Locate every Plasmodium parasite and every leukocyte.
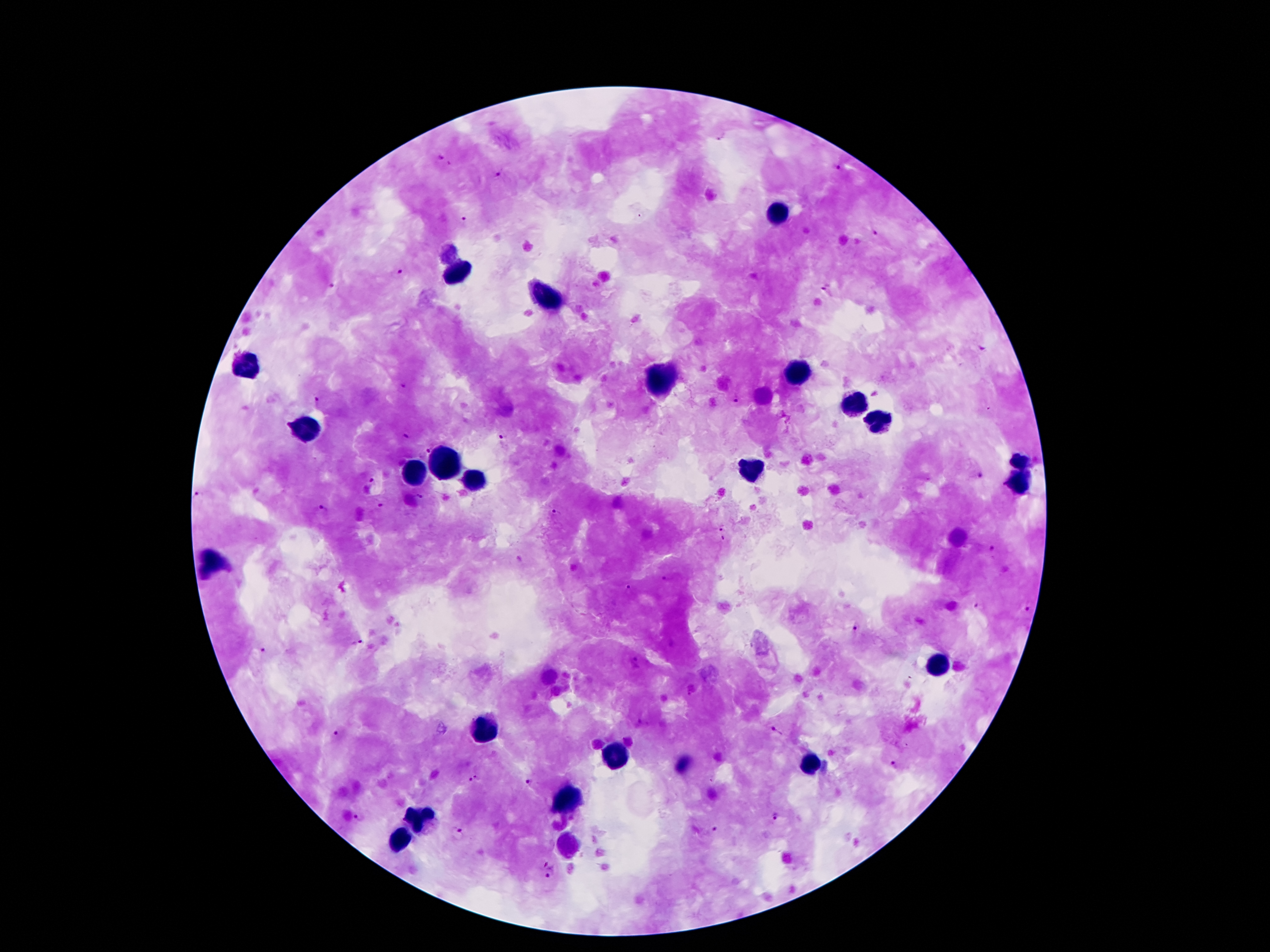

Approximate centers as (x, y) in pixels.
Plasmodium parasites: (721, 135), (438, 158), (839, 169), (500, 174), (462, 220), (874, 233), (400, 271), (336, 287), (824, 289), (980, 347), (402, 385), (737, 400), (317, 402), (406, 437), (503, 439), (428, 448), (980, 477), (372, 480), (201, 497), (419, 498), (380, 506), (324, 510), (557, 513), (720, 527), (724, 538), (992, 549), (665, 578), (628, 589), (979, 606), (1027, 609), (856, 627), (356, 642), (262, 652), (634, 662), (689, 694), (777, 732), (339, 733), (894, 767), (474, 779), (530, 783), (775, 815), (360, 817), (715, 829), (458, 831), (551, 872).
Leukocytes: (776, 211), (455, 274), (547, 297), (247, 362), (797, 371), (661, 377), (856, 398), (877, 423), (310, 427), (442, 461), (1020, 461), (751, 469), (415, 472), (472, 484), (1020, 484), (211, 564), (936, 667), (484, 732), (618, 753), (807, 765), (563, 805), (423, 818), (400, 837), (567, 844).

Image is 1270×952 pixels. 100x magnification. Single field of view. Giemsa stain. Patient malaria status: infected with Plasmodium falciparum. Smartphone photograph taken through the microscope eyepiece. Thick peripheral-blood smear.